Report the malaria status of this cell.
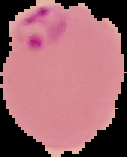
Parasitized.

Summary:
  - Image type: cell region segmented out of the field of view; surrounding area masked to black
  - Image size: 127×157 pixels
  - Preparation: thin blood film